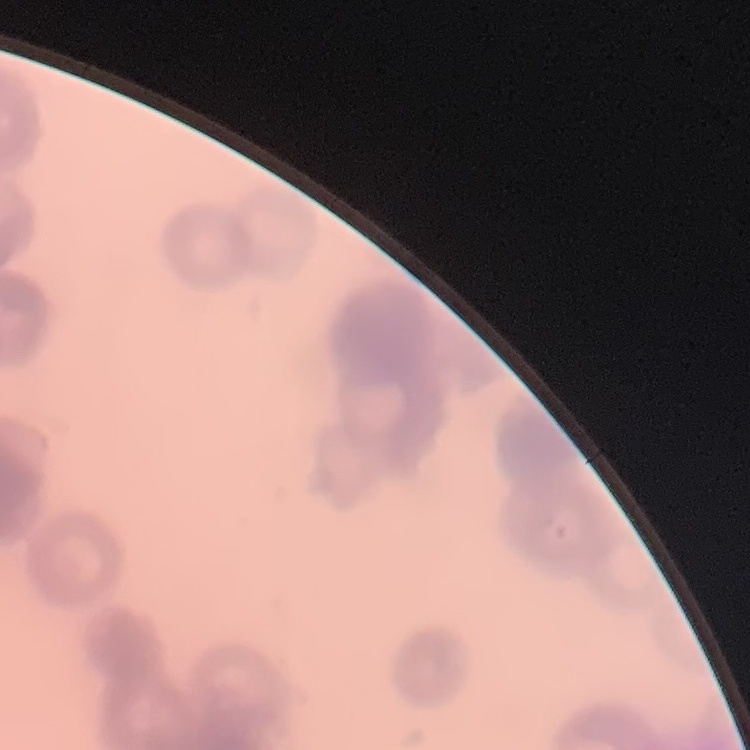

The erythrocytes exhibit rouleaux formation. Thin blood smear. Stained with either Field's or Giemsa. One tile cut from a larger photomicrograph.